Draw a bounding box around every parasitised red blood cell, every trophozoite, every gametocyte, every leukocyte, and every artifact (platelet-like body, stain precipitate, or debris).
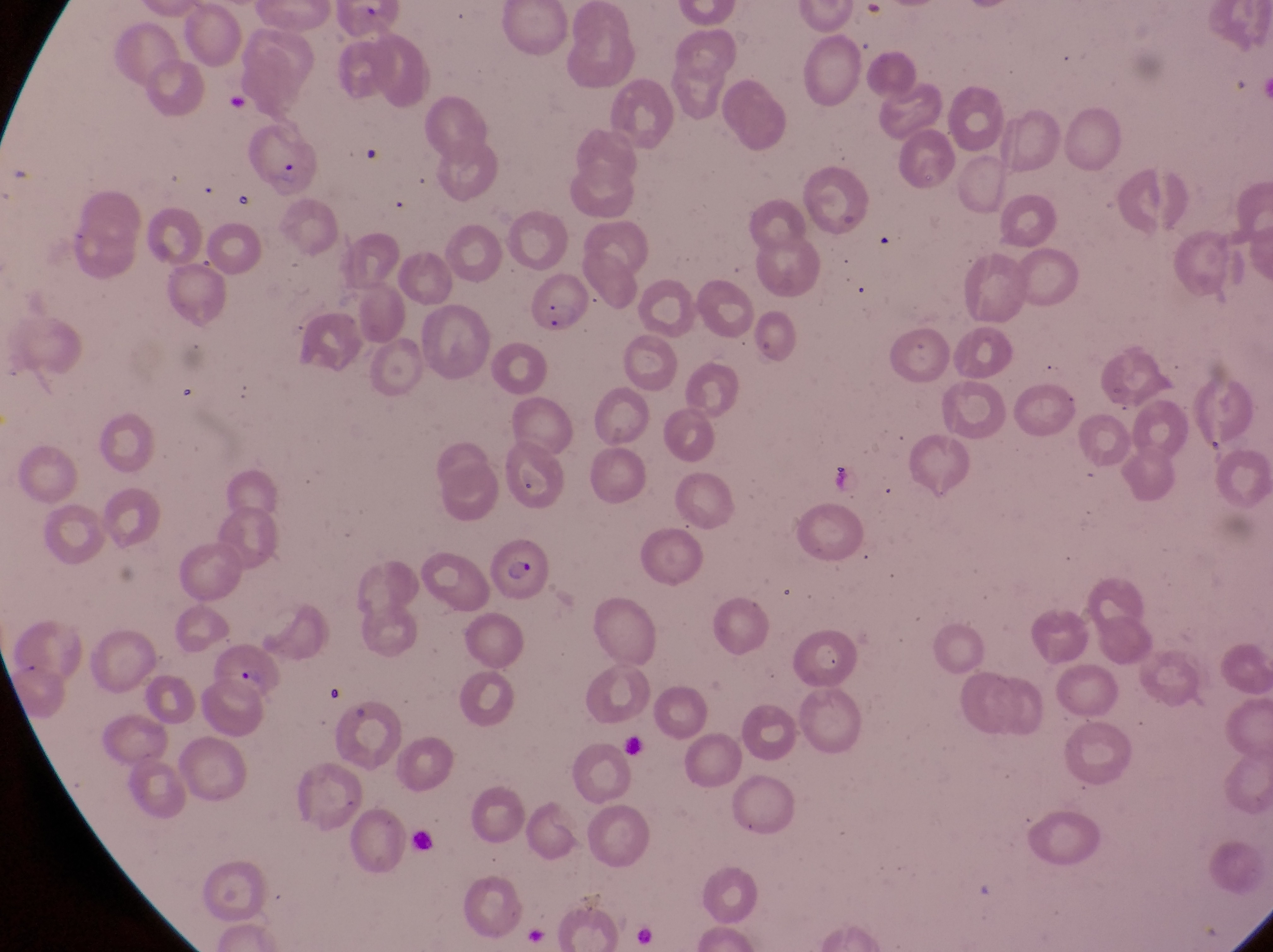

Approximate bounding boxes as [left, top, right, bottom] in pixels.
Parasitised red blood cells: [245, 134, 325, 199], [524, 270, 593, 337], [486, 544, 548, 604], [210, 640, 293, 712].
No leukocytes observed.

image size = 1273×952 pixels
field of view = single
capture = smartphone photograph through the eyepiece of an Olympus CX-23 microscope
country = Uganda
preparation = thin blood film
magnification = 1000x